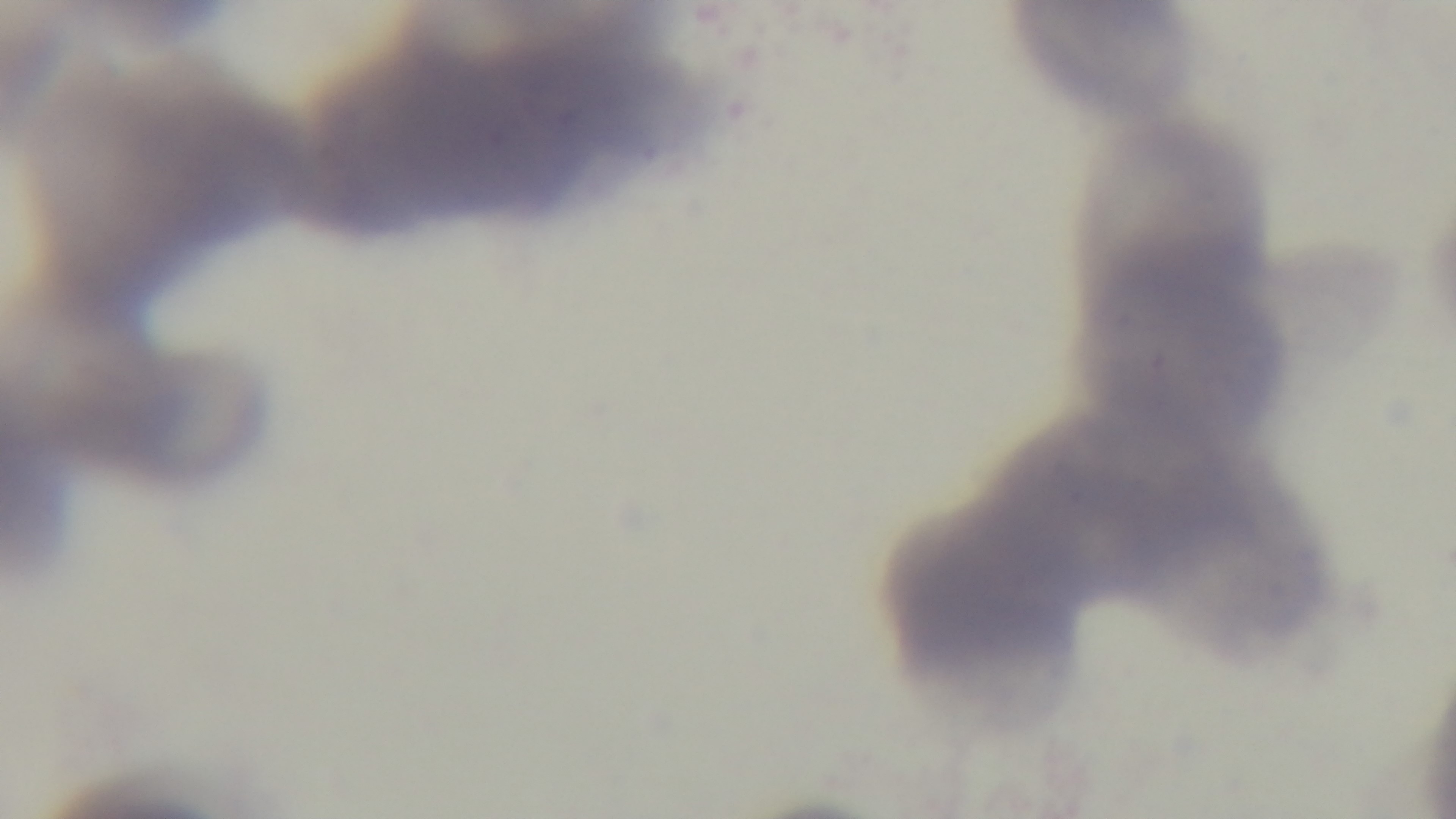
Summary:
  - Objective: 100x oil immersion
  - Modality: light microscopy
  - Preparation: thin smear
  - Field of view: one from the slide
  - Capture: mounted 4K digital camera
  - Stain: Giemsa
  - Malaria status: uninfected